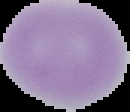
{
  "result": "no Plasmodium parasites detected",
  "image_type": "segmented cell region with the area outside set to black",
  "image_size": "130×112 pixels",
  "preparation": "thin blood smear"
}